Locate every leukocyte (white blood cell).
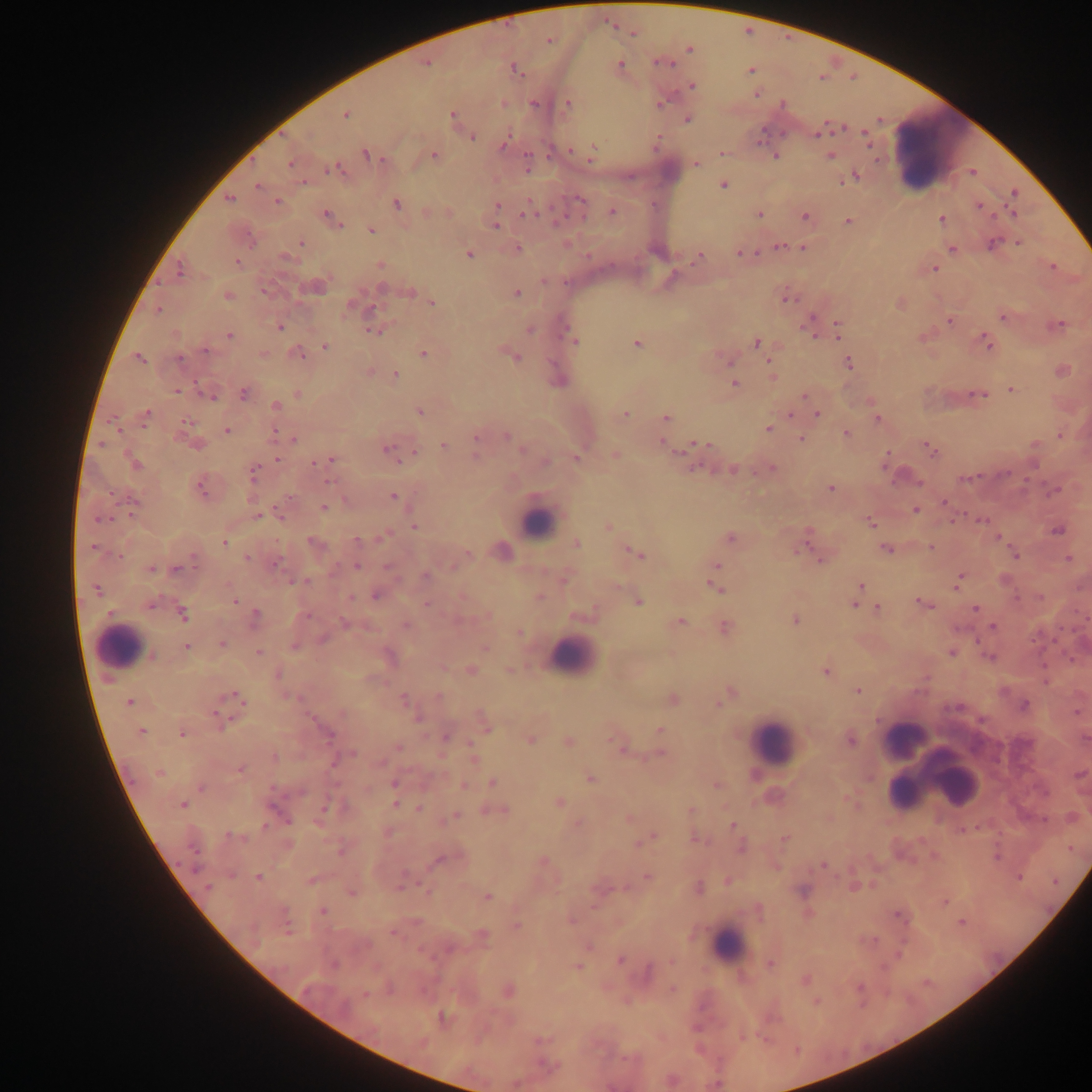
Approximate centers as [x, y] in pixels.
Leukocytes: [936, 147], [536, 521], [120, 646], [572, 656], [904, 740], [772, 742], [918, 752], [933, 777], [955, 781], [729, 948].

{
  "plasmodium_parasite_locations": "approximate centers as [x, y] in pixels: [632, 33], [548, 39], [689, 49], [661, 61], [425, 62], [619, 65], [514, 69], [750, 70], [692, 85], [756, 93], [568, 103], [345, 114], [453, 114], [687, 118], [819, 132], [865, 135], [472, 136], [504, 142], [571, 150], [721, 153], [365, 154], [592, 154], [433, 155], [775, 155], [830, 156], [291, 163], [695, 163], [527, 167], [335, 168], [972, 172], [855, 175], [842, 181], [303, 182], [722, 183], [257, 185], [1014, 193], [229, 198], [276, 202], [396, 204], [498, 206], [978, 206], [611, 211], [1013, 213], [526, 214], [759, 214], [804, 217], [330, 218], [942, 219], [848, 221], [495, 224], [370, 230], [1017, 242], [300, 243], [992, 244], [779, 246], [517, 248], [803, 248], [951, 249], [468, 253], [740, 253], [699, 257], [285, 258], [237, 262], [380, 264], [1052, 267], [934, 268], [179, 270], [315, 286], [409, 291], [516, 292], [227, 296], [785, 298], [431, 302], [900, 303], [351, 304], [158, 310], [1003, 315], [950, 320], [837, 323], [1057, 324], [279, 326], [375, 329], [530, 330], [811, 330], [838, 330], [229, 335], [837, 336], [922, 337], [574, 342], [987, 342], [636, 343], [756, 343], [326, 346], [298, 353], [262, 354], [423, 354], [511, 354], [139, 358], [728, 360], [771, 362], [848, 363], [1061, 370], [370, 372], [395, 375], [772, 378], [734, 384], [1011, 388], [176, 390], [243, 393], [979, 393], [210, 394], [297, 394], [804, 394], [871, 400], [275, 407], [419, 411], [791, 413], [622, 414], [817, 414], [145, 415], [665, 417], [877, 418], [185, 423], [768, 428], [664, 429], [227, 430], [275, 433], [846, 434], [506, 435], [1060, 435], [476, 436], [293, 439], [801, 439], [662, 441], [196, 443], [697, 443], [1033, 444], [477, 445], [443, 446], [927, 447], [388, 449], [614, 454], [477, 455], [277, 458], [575, 458], [329, 460], [886, 461], [544, 462], [320, 463], [134, 464], [732, 468], [770, 468], [253, 472], [202, 486], [830, 487], [1055, 490], [392, 496], [944, 502], [323, 507], [916, 510], [280, 512], [257, 514], [981, 520], [870, 522], [414, 525], [608, 526], [1058, 529], [382, 535], [998, 537], [730, 538], [806, 538], [357, 540], [223, 542], [314, 544], [576, 544], [931, 547], [886, 548], [500, 550], [637, 553], [1015, 554], [249, 557], [1068, 558], [821, 560], [275, 562], [356, 565], [150, 568], [716, 568], [177, 569], [425, 576], [563, 578], [1004, 579], [959, 581], [716, 586], [859, 586], [376, 595], [1039, 596], [539, 597], [234, 601], [637, 601], [921, 602], [855, 603], [869, 605], [877, 607], [976, 609], [182, 613], [255, 617], [795, 619], [680, 621], [345, 623], [406, 625], [994, 626], [724, 627], [519, 633], [222, 644], [187, 646], [485, 647], [950, 651], [258, 652], [388, 656], [990, 656], [442, 668], [510, 669], [470, 670], [825, 670], [278, 673], [857, 690], [729, 693], [233, 699], [403, 699], [671, 699], [129, 701], [719, 702], [1023, 705], [418, 716], [484, 724], [659, 730], [142, 731], [182, 733], [446, 737], [1085, 738], [529, 739], [850, 739], [568, 741], [619, 745], [398, 747], [472, 750], [659, 753], [351, 754], [274, 757], [473, 758], [240, 768], [160, 772], [1079, 774], [590, 778], [492, 782], [394, 783], [463, 784], [717, 785], [846, 799], [396, 802], [558, 802], [182, 804], [324, 808], [419, 808], [494, 810], [691, 810], [454, 816], [629, 818], [578, 823], [733, 825], [962, 829], [694, 837], [647, 838], [785, 838], [740, 847], [340, 849], [440, 858], [542, 862], [823, 865], [776, 866], [647, 876], [259, 877], [1018, 877], [312, 879], [727, 880], [402, 881], [853, 887], [698, 888], [351, 891], [486, 897], [944, 902], [758, 910], [322, 912], [571, 919], [961, 922], [516, 926], [392, 932], [481, 936], [590, 946], [620, 959], [769, 964], [576, 967], [804, 979], [672, 989], [508, 991], [365, 994], [816, 1001], [443, 1018], [671, 1080], [515, 1083]",
  "country": "Ghana",
  "capture": "mobile-phone photograph through a microscope",
  "image_size": "1092×1092 pixels",
  "field_of_view": "single",
  "preparation": "thick blood film"
}